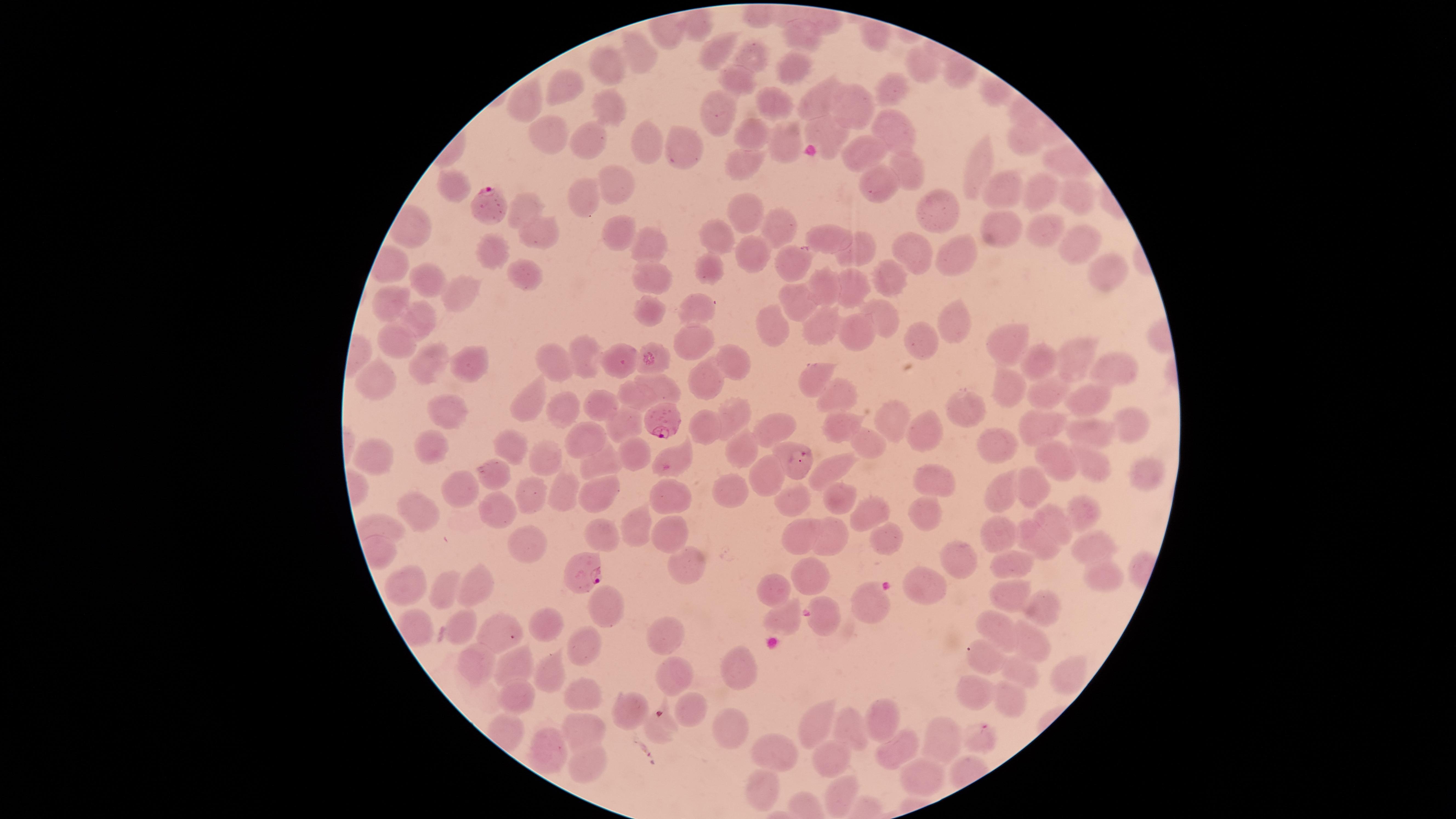

Approximate marker points as {x, y} in pixels.
Summary:
  - Uninfected RBCs: {800, 35}, {720, 53}, {636, 56}, {754, 60}, {607, 65}, {924, 66}, {792, 72}, {736, 78}, {896, 80}, {565, 90}, {816, 101}, {772, 102}, {524, 104}, {607, 104}, {861, 104}, {719, 112}, {898, 128}, {752, 134}, {547, 135}, {822, 135}, {588, 139}, {1018, 142}, {649, 143}, {785, 144}, {681, 146}, {864, 150}, {746, 160}, {1059, 164}, {905, 165}, {981, 167}, {623, 180}, {871, 184}, {994, 185}, {456, 186}, {1074, 194}, {1035, 195}, {582, 196}, {528, 205}, {751, 212}, {941, 214}, {783, 225}, {616, 226}, {1002, 229}, {1047, 229}, {715, 232}, {540, 238}, {1079, 238}, {832, 239}, {646, 244}, {917, 248}, {864, 250}, {755, 253}, {489, 254}, {969, 257}, {787, 262}, {711, 266}, {647, 272}, {1103, 272}, {522, 273}, {890, 278}, {436, 282}, {825, 286}, {850, 288}, {465, 291}, {794, 299}, {389, 303}, {652, 309}, {704, 310}, {883, 312}, {415, 314}, {954, 319}, {775, 320}, {819, 330}, {696, 336}, {853, 336}, {397, 338}, {918, 340}, {1001, 347}, {585, 353}, {1080, 358}, {616, 359}, {1036, 360}, {659, 364}, {730, 364}, {428, 365}, {1111, 365}, {469, 366}, {562, 366}, {814, 375}, {381, 379}, {708, 382}, {662, 384}, {1002, 392}, {839, 393}, {1044, 393}, {634, 396}, {536, 399}, {1092, 399}, {601, 404}, {964, 405}, {451, 407}, {563, 408}, {738, 412}, {898, 420}, {1129, 421}, {624, 422}, {1036, 425}, {842, 426}, {708, 427}, {777, 428}, {928, 428}, {1097, 435}, {586, 437}, {428, 442}, {863, 442}, {503, 443}, {1001, 446}, {743, 450}, {636, 453}, {675, 454}, {373, 456}, {1053, 456}, {792, 458}, {544, 460}, {1082, 461}, {604, 462}, {490, 470}, {828, 471}, {775, 476}, {1142, 476}, {929, 477}, {1036, 481}, {564, 491}, {452, 493}, {733, 493}, {997, 495}, {533, 498}, {671, 498}, {598, 501}, {797, 501}, {845, 501}, {1079, 511}, {421, 514}, {497, 514}, {873, 515}, {927, 516}, {1051, 521}, {638, 530}, {671, 530}, {828, 532}, {598, 535}, {1002, 535}, {802, 537}, {887, 542}, {1040, 542}, {521, 545}, {1091, 546}, {960, 558}, {1007, 564}, {684, 566}, {811, 571}, {1102, 575}, {922, 586}, {409, 588}, {775, 590}, {1007, 592}, {480, 593}, {443, 594}, {870, 601}, {1037, 603}, {609, 611}, {784, 619}, {824, 621}, {552, 625}, {997, 627}, {465, 628}, {501, 631}, {667, 638}, {1034, 645}, {577, 648}, {978, 657}, {478, 664}, {732, 664}, {524, 666}, {1024, 670}, {1066, 672}, {551, 673}, {671, 678}, {975, 694}, {1010, 694}, {580, 698}, {517, 699}, {694, 709}, {631, 712}, {814, 721}, {886, 723}, {726, 728}, {853, 729}, {584, 730}, {659, 730}, {941, 741}, {979, 743}, {777, 752}, {899, 752}, {547, 753}, {831, 758}, {591, 768}, {923, 777}, {763, 792}, {840, 797}
  - Parasitized RBCs: {493, 211}, {666, 418}, {581, 566}
  - Species: Plasmodium falciparum
  - Image size: 1456×819 pixels
  - Field of view: single
  - Preparation: thin blood film
  - Visible region: circular
  - Stain: Giemsa
  - Presence: malaria parasites seen
  - Capture: smartphone photograph through the microscope eyepiece